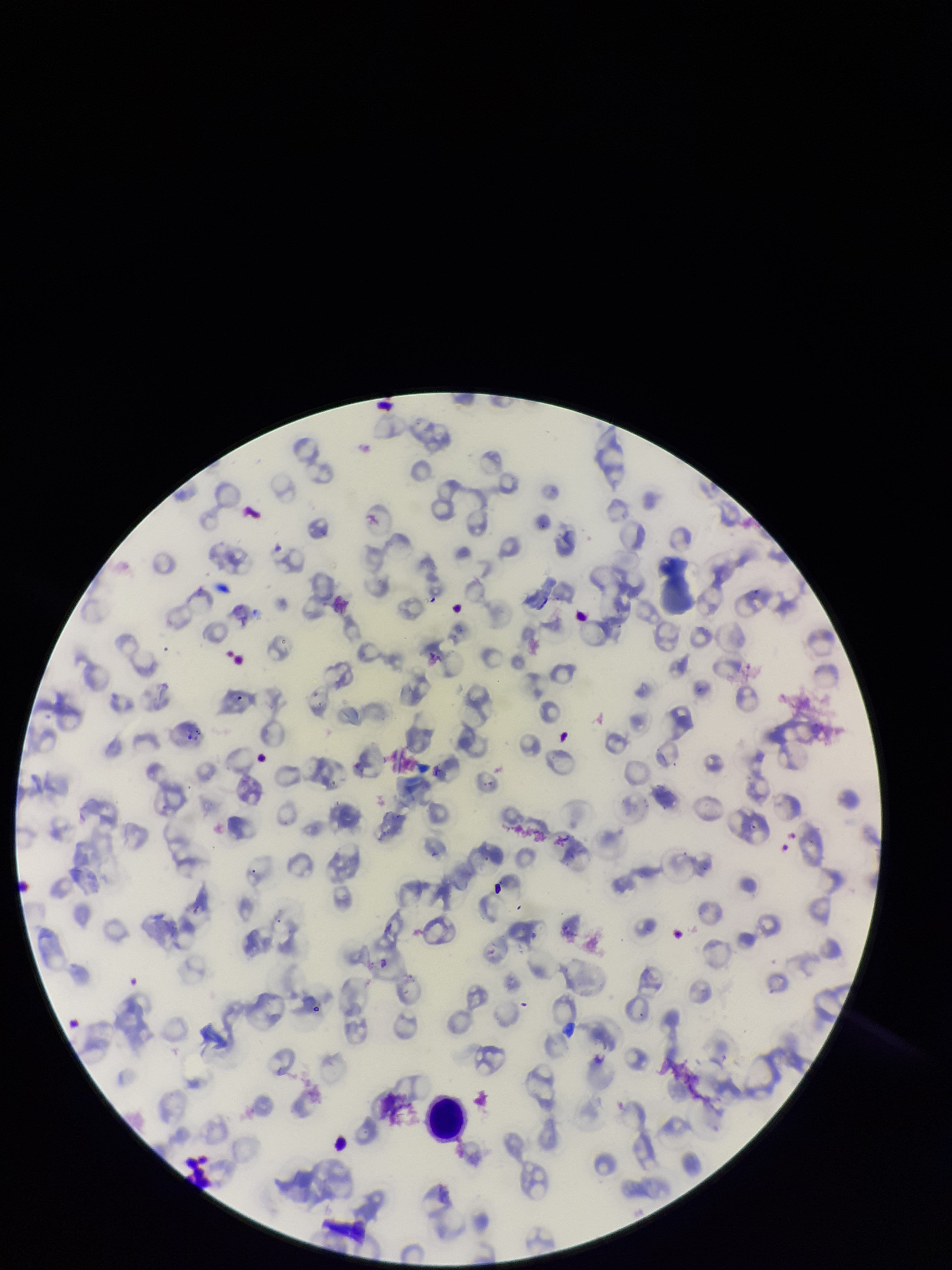
preparation = thin
patient malaria status = infected
capture = smartphone photograph through the microscope eyepiece
field of view = one from this slide
image size = 952×1270 pixels
stain = Giemsa
parasitized red blood cells = none identified
red blood cell count = 94
species reported for this patient = Plasmodium falciparum
parasitized red blood cell count = 0